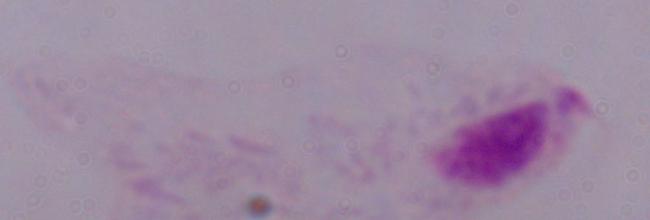

Summary:
  - Modality: micrograph
  - Identification: trichomonad
  - Magnification: 1000x